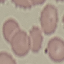
Result: no malaria parasites seen. Cell patch, automatically extracted from a larger field of view and resized to 64 × 64 pixels. Thin smear of blood. Acquired by smartphone through the microscope eyepiece. Giemsa stain.